Locate platelets.
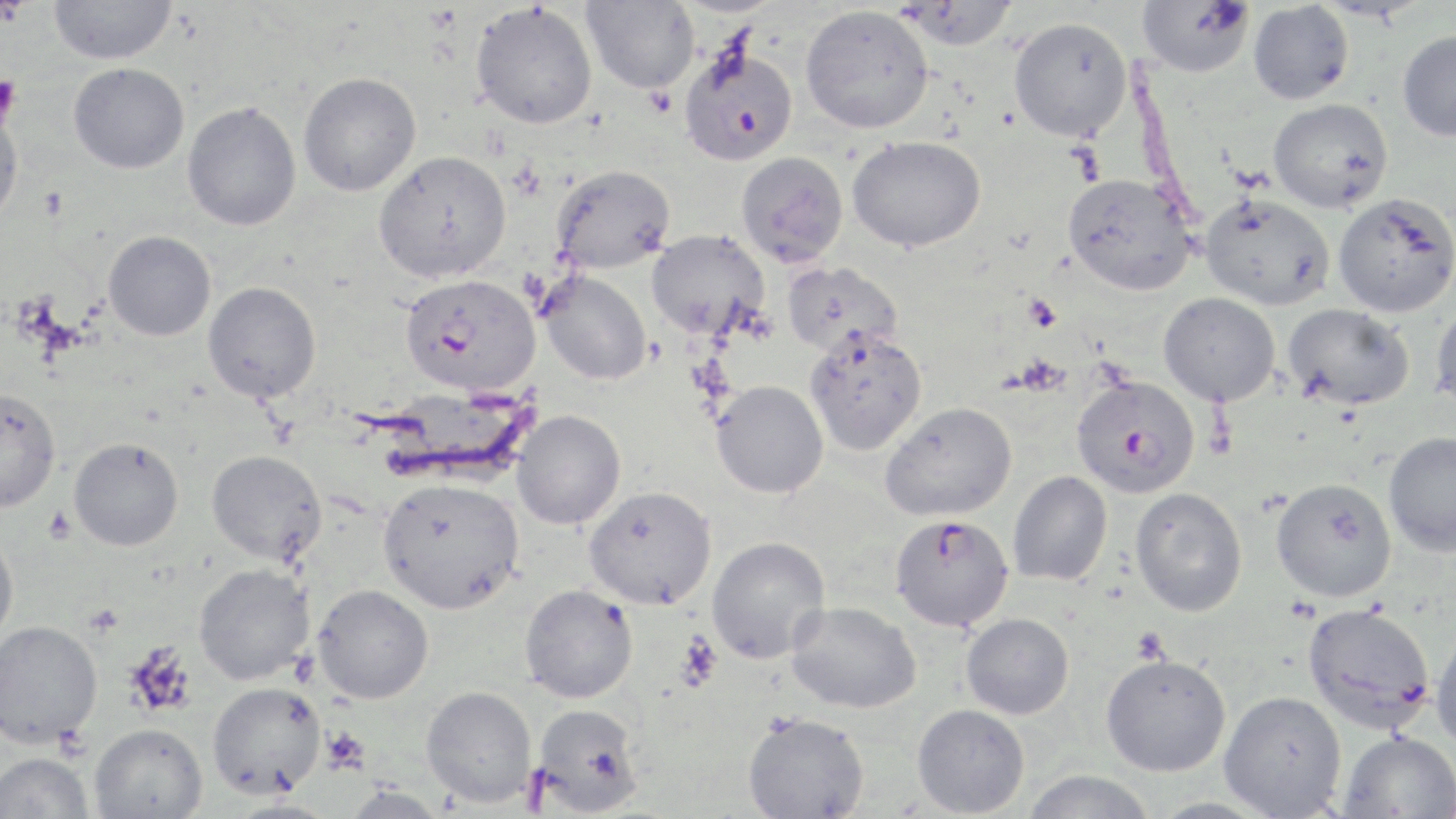

Approximate bounding boxes as (x1,y1)-(x2,y2) corner pairs in pixels.
Platelets: (0,73)-(20,126), (39,188)-(69,221), (44,507)-(76,543), (86,604)-(122,635), (1131,627)-(1169,664), (675,634)-(722,691), (322,728)-(368,774).

slide_level_diagnosis: Plasmodium falciparum
magnification: 1000x
preparation: thin blood smear
modality: optical microscopy
stain: May-Grünwald-Giemsa
image_size: 1456×819 pixels
uninfected_red_blood_cell_locations: 'approximate bounding boxes as (x1,y1)-(x2,y2) corner pairs in pixels: (48,0)-(177,65), (582,0)-(699,93), (895,0)-(1019,52), (1138,0)-(1255,77), (470,2)-(598,129), (1248,2)-(1354,104), (801,5)-(933,134), (1008,16)-(1132,142), (1397,30)-(1456,142), (68,62)-(189,173), (298,72)-(421,196), (1268,98)-(1393,212), (183,102)-(301,231), (0,107)-(24,226), (847,135)-(986,252), (373,150)-(511,283), (735,152)-(848,267), (552,163)-(676,272), (1062,173)-(1196,294), (1333,192)-(1456,317), (1200,194)-(1334,310), (103,230)-(216,341), (646,230)-(769,338), (782,260)-(903,356), (539,271)-(653,385), (203,281)-(321,403), (1158,292)-(1280,405), (1430,303)-(1456,411), (1284,304)-(1415,410), (804,327)-(927,455), (375,381)-(524,491), (711,381)-(829,498), (0,388)-(61,512), (881,401)-(1017,521), (511,410)-(626,529), (1383,430)-(1456,556), (68,437)-(184,551), (206,450)-(326,563), (1007,470)-(1113,585), (377,476)-(524,614), (1271,478)-(1397,601), (584,484)-(717,609), (1130,487)-(1247,616), (0,530)-(19,649), (706,536)-(831,663), (193,563)-(315,685), (313,584)-(434,703), (519,584)-(638,703), (786,601)-(922,713), (961,613)-(1074,720), (0,620)-(102,748), (1431,625)-(1456,755), (1100,652)-(1231,776), (207,681)-(326,799), (422,685)-(537,808), (1219,690)-(1347,817), (912,703)-(1030,817), (532,704)-(643,816), (742,711)-(869,818), (89,722)-(207,818), (1338,730)-(1456,819), (0,751)-(95,818), (1021,769)-(1156,819), (341,784)-(449,819)'
plasmodium_falciparum_infected_red_blood_cell_locations: 'approximate bounding boxes as (x1,y1)-(x2,y2) corner pairs in pixels: (679,46)-(798,165), (400,273)-(540,396), (1071,374)-(1201,498), (889,514)-(1014,631), (1301,602)-(1436,732)'
field_of_view: one of a larger specimen